State which parasite is depicted.
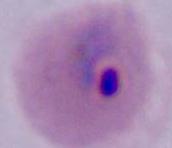

Plasmodium.

{
  "magnification": "400x or 1000x",
  "modality": "micrograph"
}